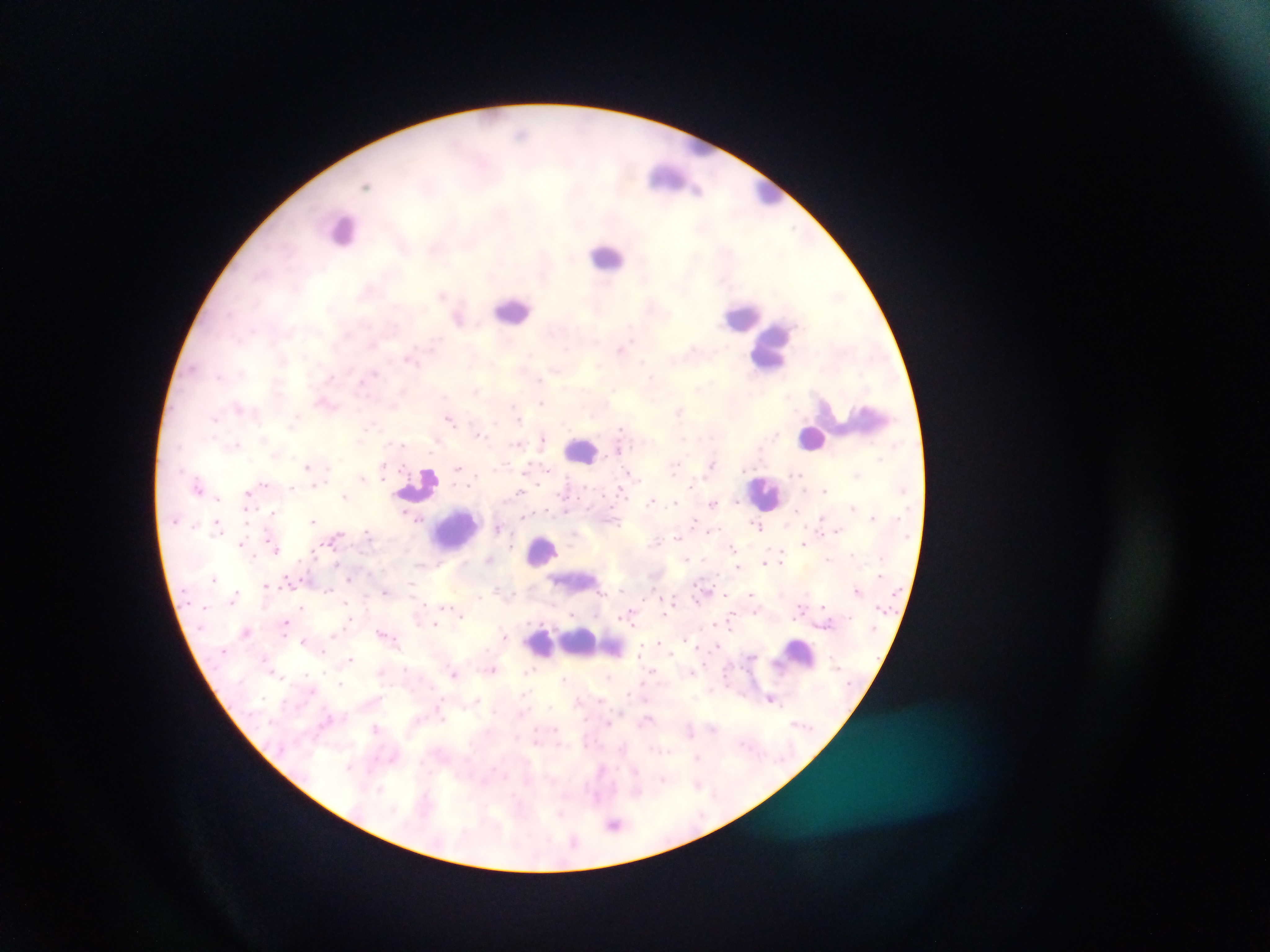

field_of_view: single
capture: mobile-phone photograph through a microscope
country: Ghana
malaria_parasite_locations: 'approximate centers as {x, y} in pixels: {442, 295}, {458, 317}, {622, 349}, {325, 400}, {542, 402}, {678, 411}, {450, 417}, {544, 438}, {619, 447}, {307, 464}, {712, 464}, {384, 465}, {529, 466}, {460, 467}, {631, 474}, {362, 478}, {264, 484}, {314, 484}, {198, 488}, {521, 491}, {248, 494}, {346, 495}, {653, 500}, {677, 501}, {735, 501}, {713, 502}, {853, 507}, {274, 510}, {407, 513}, {524, 517}, {313, 519}, {695, 519}, {822, 519}, {217, 522}, {758, 526}, {498, 527}, {837, 529}, {710, 530}, {368, 532}, {678, 535}, {242, 543}, {804, 543}, {733, 548}, {275, 549}, {783, 552}, {255, 556}, {686, 558}, {490, 559}, {764, 562}, {338, 563}, {737, 567}, {349, 578}, {287, 579}, {266, 585}, {857, 589}, {329, 590}, {385, 591}, {727, 593}, {750, 593}, {480, 597}, {233, 599}, {696, 600}, {303, 606}, {822, 607}, {799, 612}, {573, 613}, {664, 614}, {462, 615}, {632, 615}, {350, 618}, {287, 621}, {435, 624}, {247, 630}, {382, 631}, {503, 636}, {304, 640}, {658, 641}, {639, 653}, {671, 653}, {351, 659}, {493, 669}, {455, 674}, {609, 675}, {565, 679}, {771, 697}, {478, 701}, {377, 728}, {535, 741}, {697, 757}, {350, 767}, {697, 783}, {614, 823}'
preparation: thick blood film
leukocyte_locations: 'approximate centers as {x, y} in pixels: {672, 181}, {769, 191}, {344, 229}, {607, 257}, {513, 309}, {742, 315}, {772, 346}, {864, 420}, {813, 438}, {581, 452}, {418, 484}, {766, 493}, {456, 528}, {542, 550}, {575, 581}, {566, 640}, {582, 640}, {799, 654}'
image_size: 1270×952 pixels